Classify this cell by malaria status.
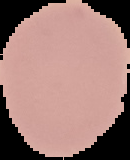
Uninfected.

image size = 130×160 pixels
preparation = thin blood smear
image type = segmented cell region with the area outside set to black